Assess this cell for malaria.
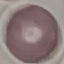
It is uninfected.

Giemsa stain. Thin blood film. Acquired by smartphone through the microscope eyepiece. Automatically extracted cell patch, resized to 64 × 64 pixels.